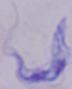 Micrograph. 1000x magnification. A trypanosome is shown.